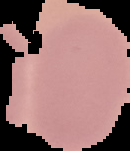
Summary:
  - Image type: segmented cell region with the area outside set to black
  - Malaria status: uninfected
  - Image size: 130×151 pixels
  - Preparation: thin blood smear